Assess the morphology of the red blood cells.
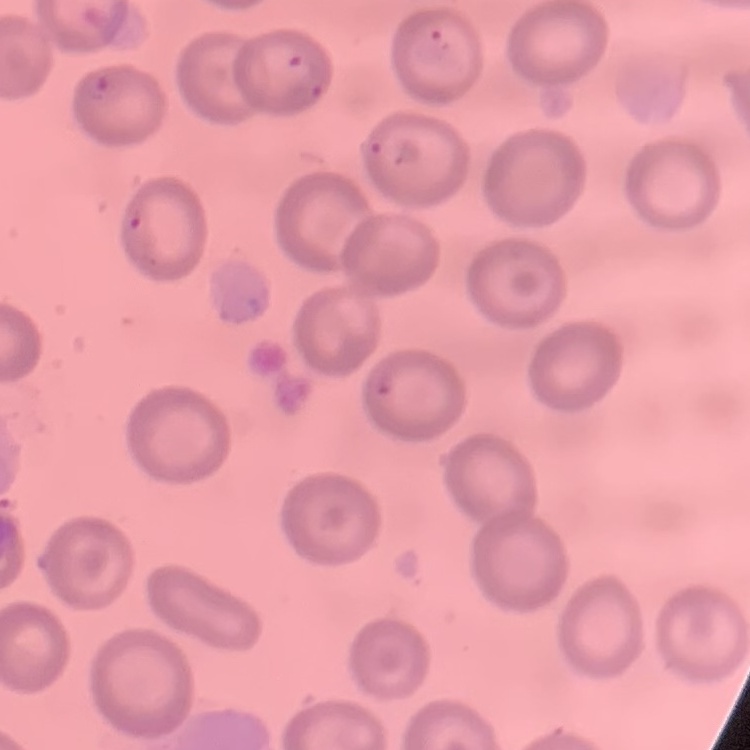

They show no rouleaux formation.

Field's or Giemsa stain. Thin blood film. Square crop of a larger photomicrograph.